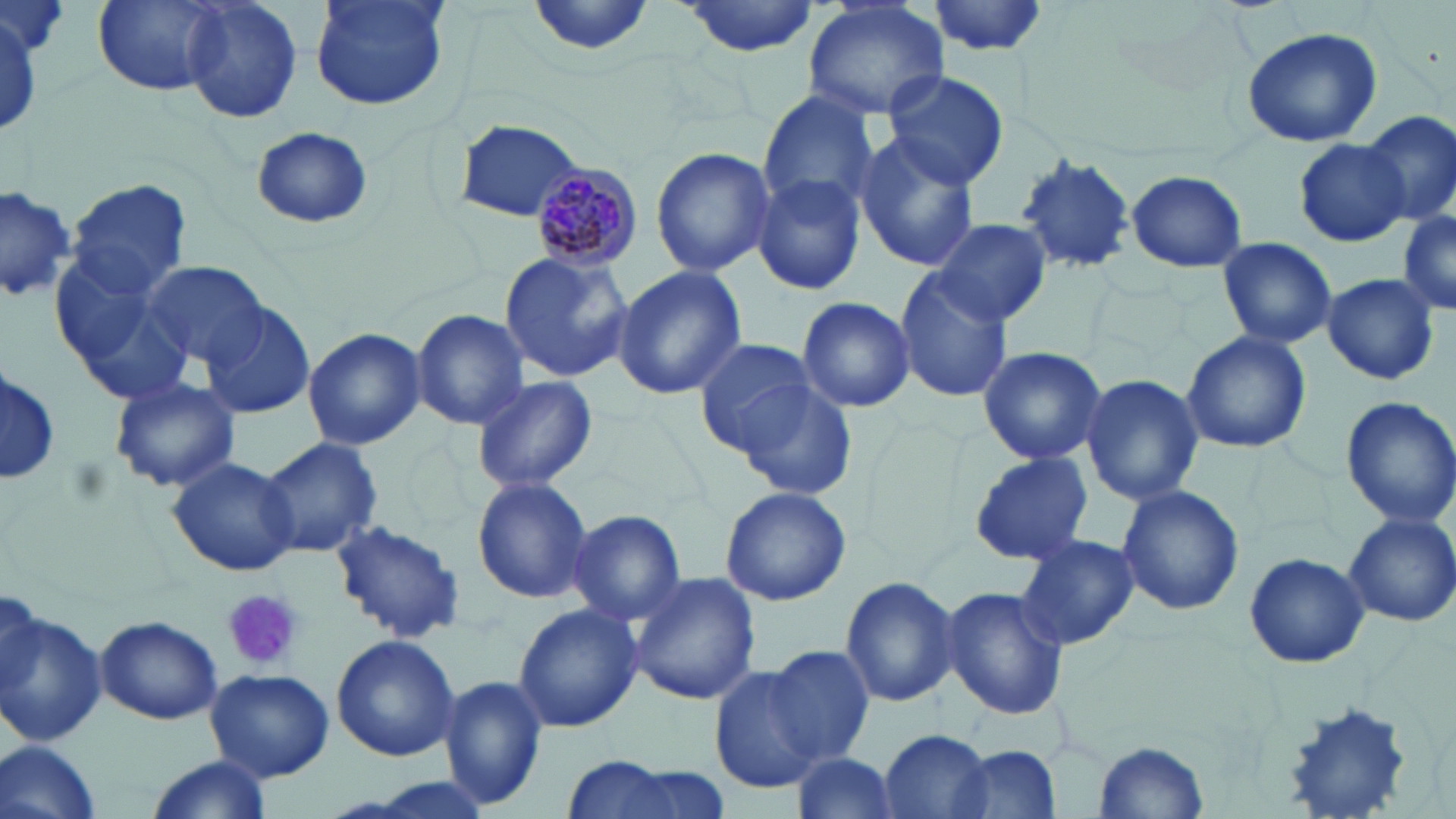

slide-level diagnosis = Plasmodium malariae
uninfected red blood cell locations = approximate bounding boxes as named x1/y1/x2/y2 corners in pixels: (x1=181, y1=0, x2=302, y2=126), (x1=309, y1=0, x2=451, y2=113), (x1=527, y1=0, x2=662, y2=58), (x1=674, y1=0, x2=822, y2=57), (x1=94, y1=1, x2=224, y2=95), (x1=803, y1=1, x2=950, y2=122), (x1=929, y1=1, x2=1052, y2=55), (x1=2, y1=9, x2=46, y2=135), (x1=1241, y1=26, x2=1383, y2=148), (x1=879, y1=69, x2=1010, y2=190), (x1=757, y1=92, x2=880, y2=216), (x1=1363, y1=110, x2=1456, y2=226), (x1=455, y1=119, x2=588, y2=223), (x1=251, y1=127, x2=373, y2=229), (x1=852, y1=133, x2=981, y2=273), (x1=1297, y1=138, x2=1410, y2=248), (x1=649, y1=147, x2=775, y2=278), (x1=1014, y1=153, x2=1133, y2=273), (x1=1125, y1=170, x2=1247, y2=273), (x1=753, y1=176, x2=867, y2=295), (x1=66, y1=180, x2=191, y2=299), (x1=0, y1=183, x2=76, y2=306), (x1=1398, y1=210, x2=1456, y2=316), (x1=935, y1=218, x2=1052, y2=326), (x1=1216, y1=236, x2=1337, y2=350), (x1=499, y1=250, x2=634, y2=384), (x1=50, y1=253, x2=193, y2=400), (x1=144, y1=259, x2=268, y2=371), (x1=612, y1=266, x2=747, y2=398), (x1=895, y1=268, x2=1013, y2=402), (x1=1321, y1=273, x2=1441, y2=385), (x1=796, y1=296, x2=915, y2=414), (x1=201, y1=304, x2=317, y2=419), (x1=410, y1=309, x2=528, y2=430), (x1=302, y1=327, x2=426, y2=450), (x1=1181, y1=330, x2=1312, y2=454), (x1=694, y1=337, x2=819, y2=452), (x1=976, y1=345, x2=1108, y2=464), (x1=1, y1=364, x2=59, y2=489), (x1=727, y1=373, x2=857, y2=497), (x1=1081, y1=374, x2=1204, y2=506), (x1=471, y1=375, x2=598, y2=493), (x1=110, y1=376, x2=240, y2=492), (x1=1340, y1=395, x2=1456, y2=528), (x1=258, y1=435, x2=382, y2=558), (x1=967, y1=451, x2=1094, y2=566), (x1=166, y1=458, x2=300, y2=576), (x1=472, y1=476, x2=592, y2=604), (x1=1116, y1=485, x2=1245, y2=616), (x1=719, y1=486, x2=851, y2=607), (x1=569, y1=509, x2=686, y2=626), (x1=1345, y1=511, x2=1456, y2=628), (x1=332, y1=519, x2=465, y2=642), (x1=1016, y1=537, x2=1141, y2=650), (x1=1244, y1=550, x2=1369, y2=670), (x1=628, y1=572, x2=761, y2=704), (x1=840, y1=573, x2=960, y2=709), (x1=941, y1=586, x2=1071, y2=722), (x1=514, y1=602, x2=643, y2=734), (x1=0, y1=606, x2=107, y2=746), (x1=94, y1=615, x2=223, y2=725), (x1=331, y1=635, x2=459, y2=760), (x1=766, y1=646, x2=875, y2=765), (x1=708, y1=664, x2=830, y2=793), (x1=204, y1=668, x2=333, y2=784), (x1=439, y1=672, x2=546, y2=811), (x1=878, y1=729, x2=996, y2=819), (x1=1093, y1=739, x2=1208, y2=814), (x1=0, y1=740, x2=102, y2=819), (x1=948, y1=745, x2=1059, y2=819), (x1=788, y1=752, x2=902, y2=819), (x1=145, y1=756, x2=273, y2=819), (x1=562, y1=756, x2=687, y2=819)
magnification = 1000x
platelet locations = approximate bounding boxes as named x1/y1/x2/y2 corners in pixels: (x1=221, y1=587, x2=304, y2=671)
field of view = single
preparation = thin blood film
image size = 1456×819 pixels
Plasmodium malariae-infected red blood cell locations = approximate bounding boxes as named x1/y1/x2/y2 corners in pixels: (x1=529, y1=164, x2=643, y2=268)
modality = light microscopy
stain = May-Grünwald-Giemsa